Report the malaria status of this cell.
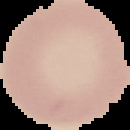

Uninfected.

Summary:
  - Preparation: thin blood smear
  - Image type: segmented cell region with the area outside set to black
  - Image size: 130×130 pixels